Report the malaria status of this cell.
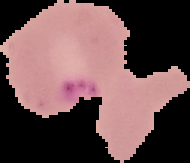
It is parasitized.

Cell region segmented out of the field of view; the surrounding area is masked to black. Image is 190×163 pixels. From a thin blood film.